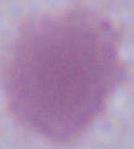
Summary:
  - Magnification: 1000x
  - Identification: red blood cell
  - Modality: photomicrograph